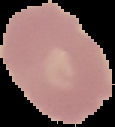

Summary:
  - Image type: segmented cell region with the area outside set to black
  - Preparation: thin blood smear
  - Result: negative for malaria parasites
  - Image size: 115×127 pixels